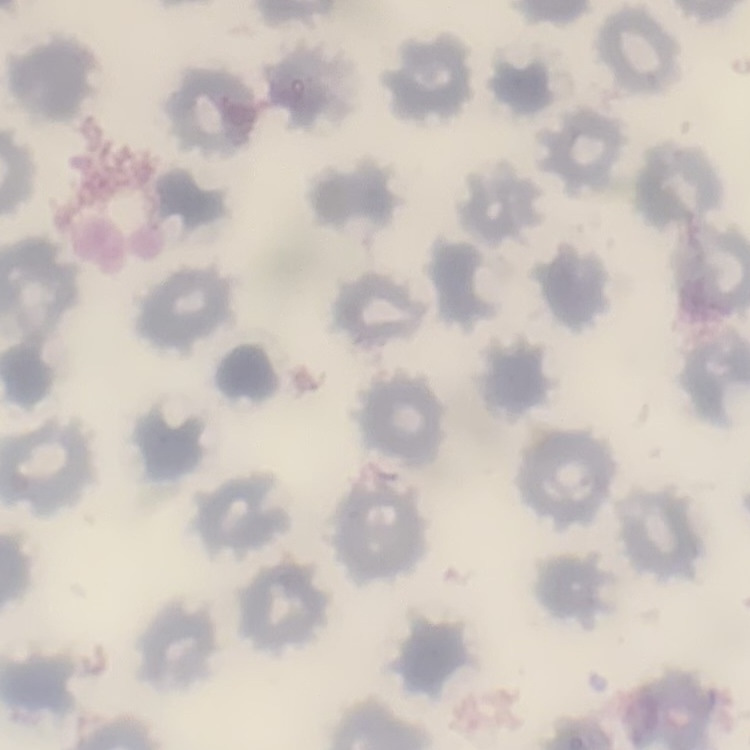

Summary:
  - Red blood cell morphology: no rouleaux formation
  - Preparation: thin blood film
  - Image type: square crop of a larger photomicrograph
  - Stain: Field's or Giemsa